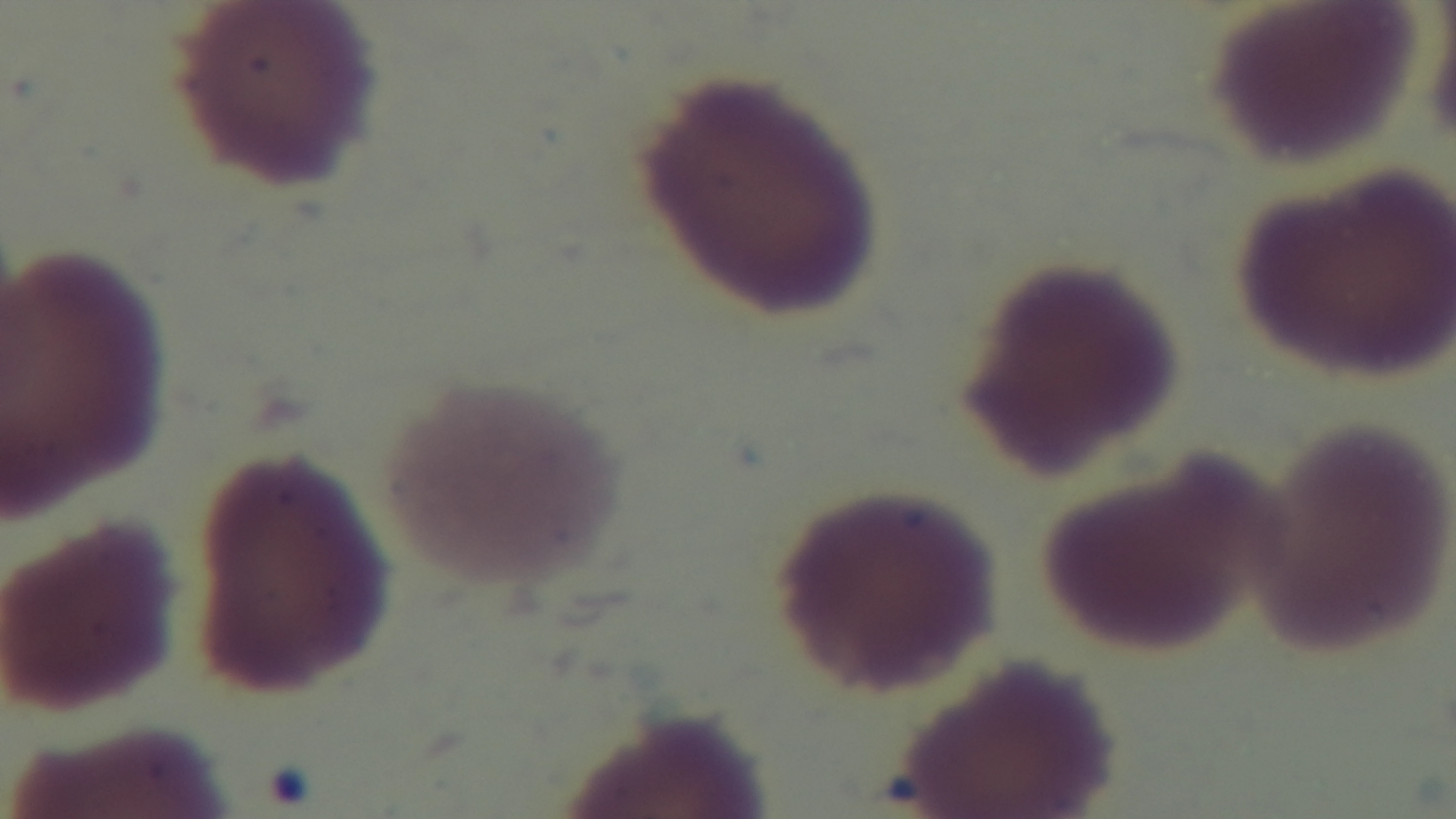

Giemsa stain. 100x oil-immersion objective. Mounted 4K digital camera. Preparation: thin. Malaria status: negative. Light microscopy. One field from the slide.